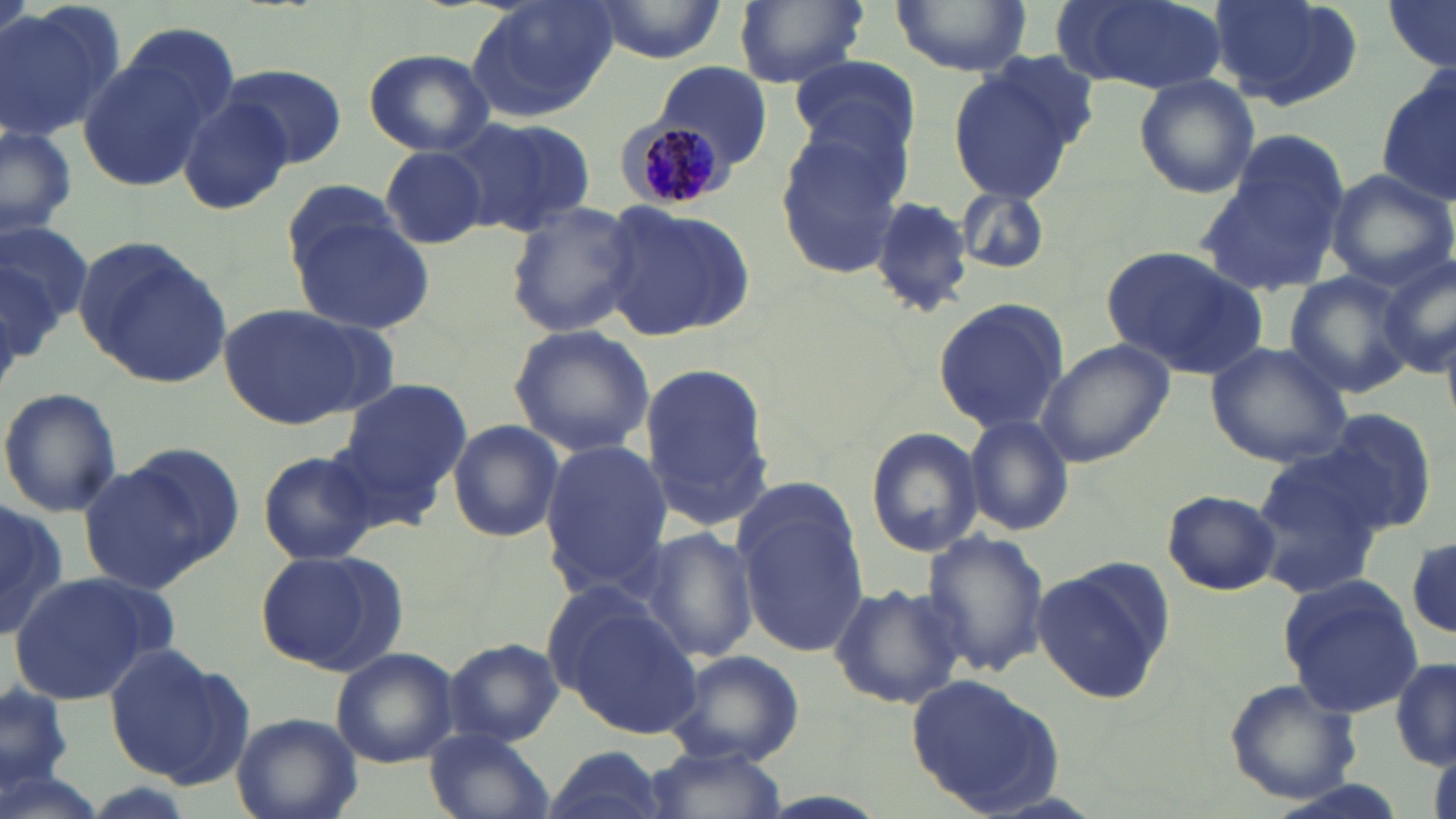
Approximate bounding boxes as (x1, y1, x2, y2) in pixels. Plasmodium malariae-infected red blood cell locations: (617, 121, 729, 213). Uninfected red blood cell locations: (466, 0, 619, 121), (586, 0, 728, 65), (734, 0, 875, 89), (891, 0, 1032, 75), (1061, 0, 1225, 93), (1205, 0, 1364, 110), (1383, 0, 1455, 71), (0, 4, 121, 143), (75, 37, 221, 191), (363, 48, 494, 157), (789, 54, 919, 161), (946, 57, 1089, 201), (657, 61, 772, 169), (221, 64, 346, 168), (1378, 69, 1456, 207), (1132, 72, 1259, 199), (177, 91, 294, 216), (446, 116, 598, 238), (0, 124, 78, 238), (774, 130, 908, 277), (1199, 141, 1351, 297), (378, 145, 489, 250), (1324, 168, 1454, 290), (282, 180, 402, 274), (954, 185, 1052, 275), (868, 196, 977, 317), (504, 199, 643, 338), (599, 201, 756, 344), (290, 215, 438, 337), (0, 220, 94, 332), (74, 237, 232, 389), (1100, 246, 1268, 379), (1375, 253, 1455, 380), (1284, 269, 1417, 398), (931, 298, 1070, 433), (222, 302, 381, 430), (508, 324, 655, 457), (1204, 340, 1354, 467), (1036, 341, 1174, 467), (636, 360, 774, 531), (335, 376, 473, 506), (1, 388, 122, 517), (1318, 405, 1443, 534), (961, 414, 1074, 537), (445, 419, 564, 543), (865, 428, 983, 557), (538, 438, 671, 593), (96, 443, 245, 582), (1246, 446, 1392, 596), (256, 449, 380, 566), (734, 488, 870, 657), (1162, 489, 1282, 596), (0, 501, 68, 641), (636, 527, 757, 663), (918, 529, 1051, 678), (1408, 536, 1455, 639), (255, 547, 407, 677), (1031, 557, 1175, 706), (10, 571, 160, 703), (1278, 574, 1424, 718), (830, 582, 967, 710), (559, 603, 702, 739), (442, 637, 562, 746), (106, 643, 251, 787), (330, 647, 459, 768), (664, 649, 805, 767), (1391, 657, 1456, 770), (905, 673, 1066, 814), (1223, 679, 1362, 805), (2, 681, 74, 798), (231, 712, 362, 819), (425, 727, 554, 819), (543, 744, 671, 819), (641, 744, 788, 819). Slide-level diagnosis: Plasmodium malariae. One field of a larger specimen. Light microscopy. Captured at 1000x magnification. May-Grünwald-Giemsa-stained preparation. Thin blood film. Image is 1456×819 pixels.